Point out every Plasmodium parasite and every leukocyte.
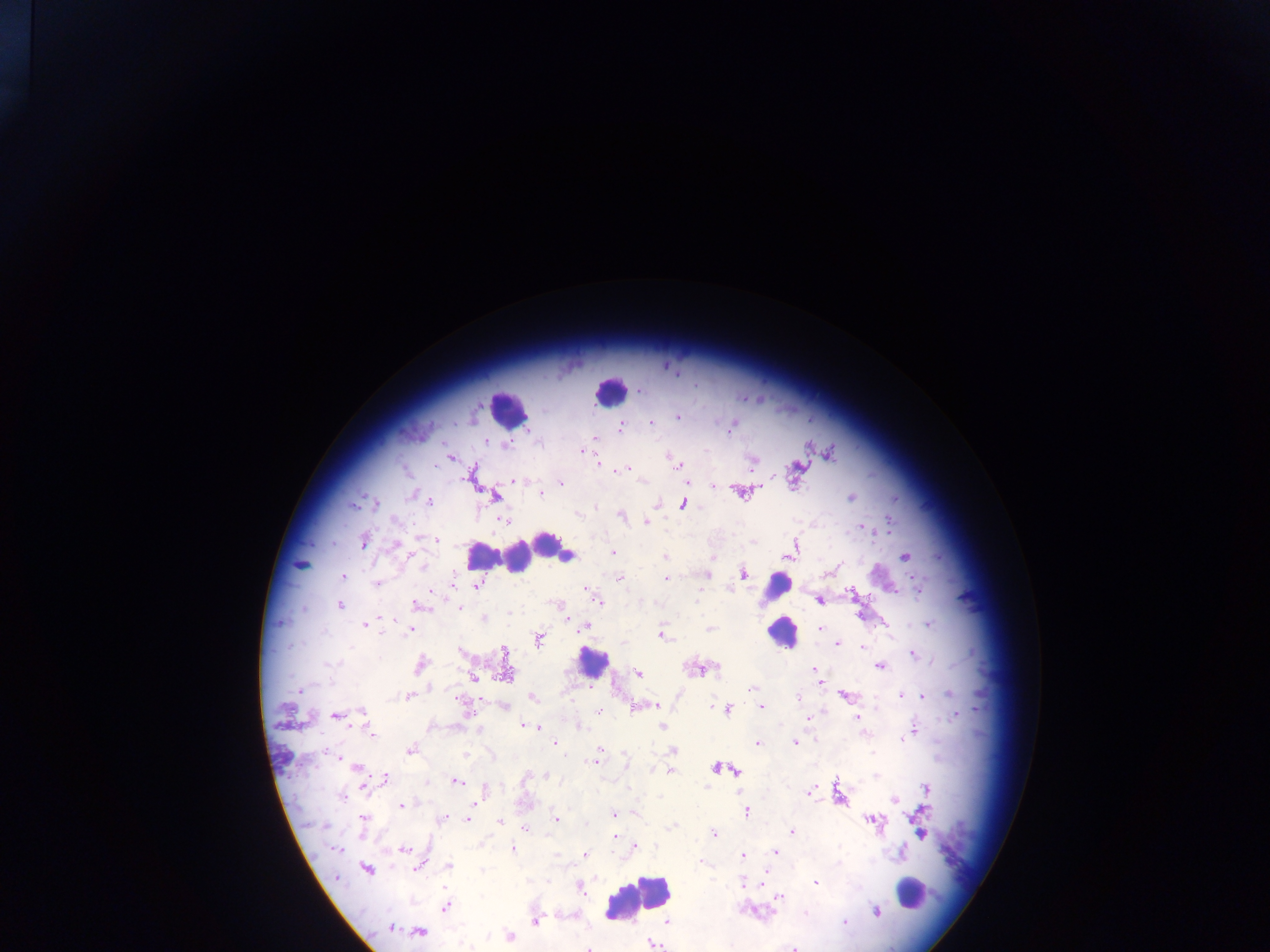

Approximate centers as {x, y} in pixels.
Plasmodium parasites: {640, 391}, {678, 417}, {652, 423}, {620, 427}, {731, 427}, {594, 438}, {487, 441}, {506, 444}, {583, 452}, {450, 458}, {597, 462}, {679, 466}, {629, 468}, {405, 469}, {614, 470}, {515, 481}, {562, 483}, {686, 483}, {712, 487}, {412, 494}, {541, 494}, {494, 496}, {851, 498}, {429, 500}, {375, 503}, {682, 504}, {353, 505}, {596, 507}, {577, 513}, {621, 516}, {502, 520}, {646, 522}, {862, 528}, {436, 540}, {364, 541}, {612, 552}, {787, 556}, {568, 557}, {905, 557}, {665, 558}, {300, 564}, {743, 572}, {707, 574}, {344, 577}, {666, 578}, {620, 579}, {376, 584}, {477, 586}, {919, 590}, {588, 591}, {852, 591}, {699, 594}, {598, 600}, {821, 600}, {339, 605}, {417, 605}, {460, 608}, {484, 619}, {366, 624}, {928, 624}, {583, 626}, {710, 628}, {820, 628}, {409, 630}, {663, 636}, {538, 640}, {624, 642}, {838, 644}, {862, 648}, {504, 652}, {912, 654}, {330, 664}, {420, 665}, {879, 667}, {815, 670}, {506, 671}, {639, 674}, {473, 676}, {820, 683}, {751, 689}, {301, 690}, {949, 694}, {901, 695}, {847, 696}, {923, 696}, {408, 697}, {799, 697}, {533, 698}, {503, 706}, {654, 706}, {711, 706}, {761, 707}, {727, 709}, {599, 711}, {362, 712}, {956, 714}, {336, 715}, {857, 717}, {808, 719}, {524, 726}, {537, 726}, {662, 726}, {579, 728}, {914, 731}, {371, 733}, {905, 738}, {555, 743}, {795, 743}, {757, 744}, {600, 749}, {410, 750}, {672, 751}, {872, 752}, {464, 755}, {335, 757}, {625, 758}, {594, 761}, {355, 767}, {716, 768}, {735, 770}, {671, 771}, {547, 776}, {385, 778}, {457, 781}, {706, 786}, {629, 789}, {926, 789}, {484, 790}, {808, 793}, {342, 796}, {893, 800}, {402, 806}, {747, 812}, {614, 813}, {364, 818}, {556, 818}, {444, 819}, {467, 819}, {870, 820}, {500, 822}, {673, 826}, {526, 830}, {791, 831}, {922, 833}, {714, 834}, {613, 837}, {635, 846}, {404, 849}, {512, 849}, {336, 850}, {775, 851}, {585, 854}, {742, 856}, {702, 862}, {838, 863}, {449, 865}, {419, 868}, {367, 869}, {483, 871}, {337, 878}, {815, 882}, {761, 883}, {742, 884}, {580, 888}, {780, 897}, {446, 906}, {805, 912}, {876, 912}, {535, 922}, {667, 922}, {845, 923}, {391, 927}, {419, 932}, {510, 936}, {653, 944}, {589, 948}, {794, 948}.
Leukocytes: {610, 391}, {507, 408}, {547, 543}, {560, 552}, {481, 555}, {518, 557}, {777, 588}, {781, 633}, {591, 662}, {911, 892}, {639, 898}.

preparation = thick blood smear
image size = 1270×952 pixels
capture = mobile-phone photograph through a microscope
field of view = single
country = Ghana